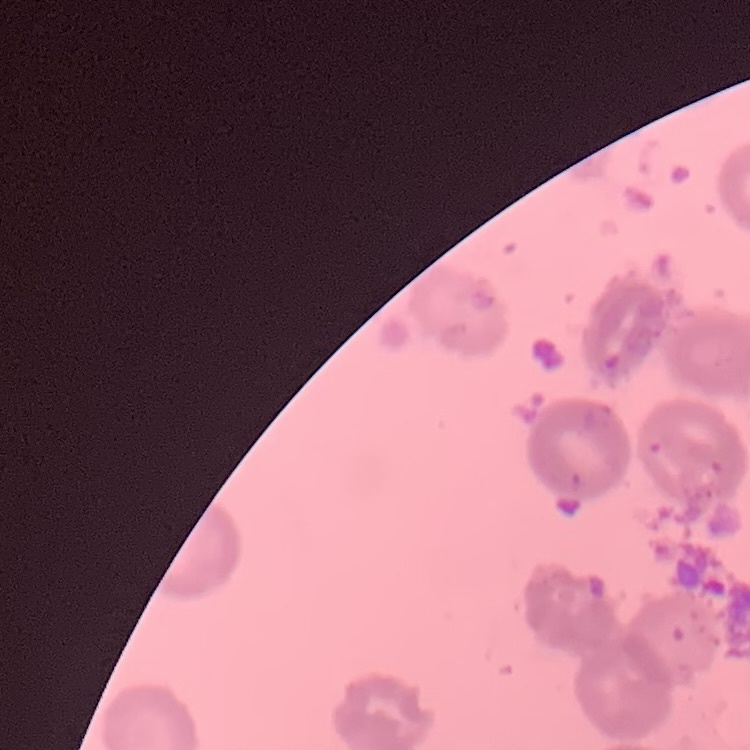 The red blood cells exhibit rouleaux formation. Thin blood smear. Square crop of a larger photomicrograph. Stained with either Field's or Giemsa.